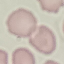
result = negative for malaria parasites
capture = smartphone camera at the microscope eyepiece
preparation = thin smear
stain = Giemsa
image type = automatically extracted cell patch, resized to 64 × 64 pixels